Describe the morphology of the erythrocytes.
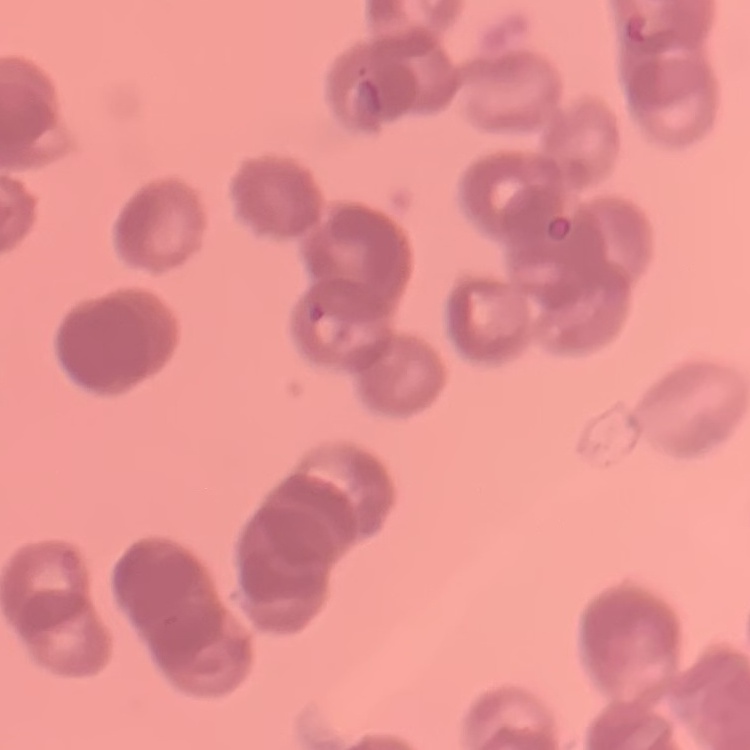
They show rouleaux formation.

preparation = thin peripheral smear
image type = square crop of a larger photomicrograph
stain = Field's or Giemsa